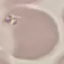
{
  "malaria_status": "uninfected",
  "preparation": "thin smear",
  "image_type": "automatically extracted cell patch, resized to 64 × 64 pixels",
  "stain": "Giemsa",
  "capture": "smartphone through the microscope eyepiece"
}